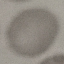

malaria status = uninfected
capture = smartphone through the microscope eyepiece
image type = cell patch, automatically extracted from a larger field of view and resized to 64 × 64 pixels
stain = Giemsa
preparation = thin blood film